Identify the cell.
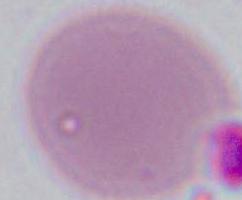

This is an erythrocyte.

modality: micrograph
magnification: 1000x